Locate every Plasmodium parasite.
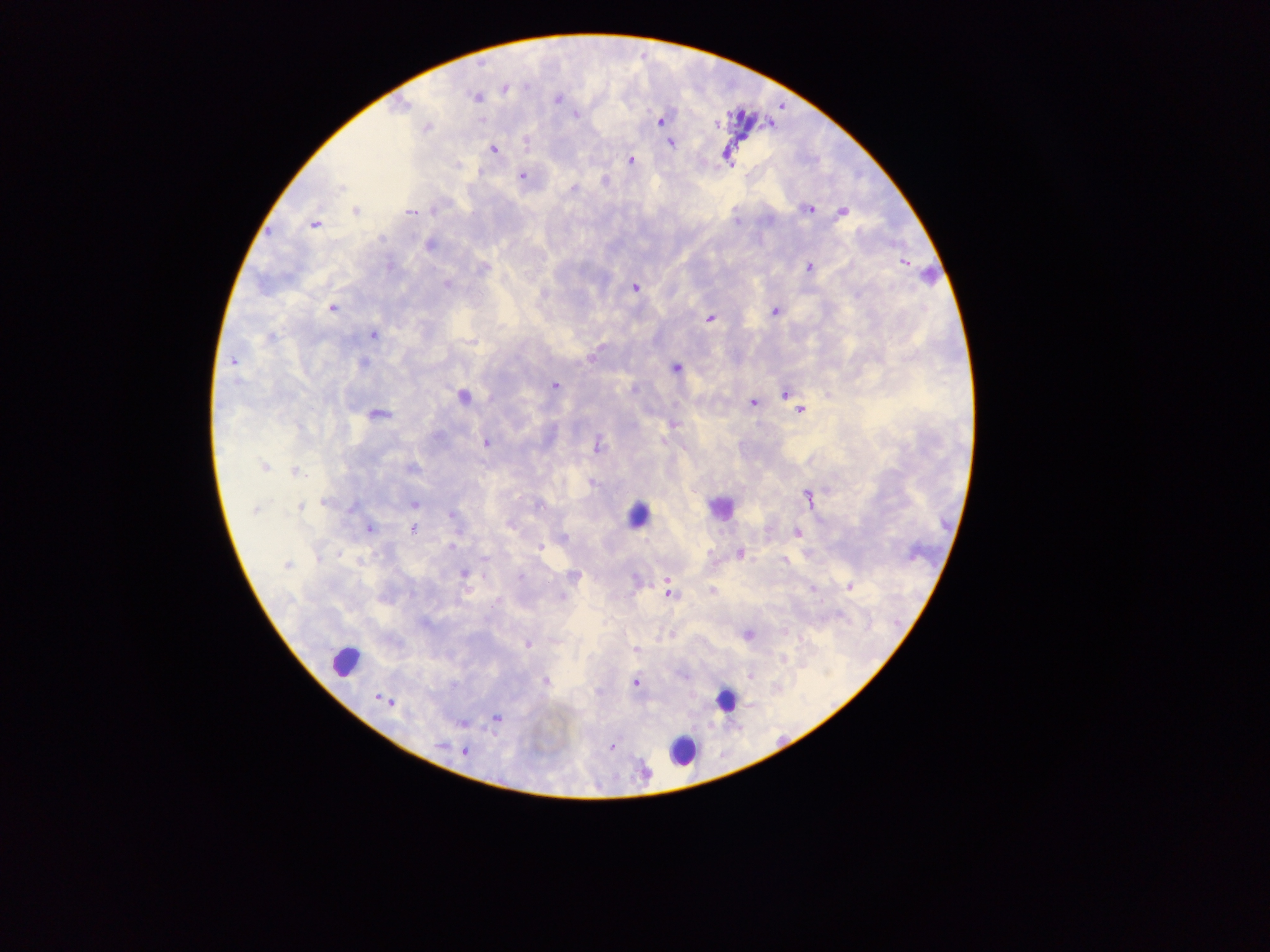

Approximate centers as (x, y) in pixels.
Plasmodium parasites: (505, 88), (476, 97), (558, 98), (401, 106), (576, 115), (481, 120), (661, 120), (717, 124), (427, 128), (526, 144), (671, 144), (494, 150), (727, 155), (631, 160), (480, 171), (522, 176), (341, 188), (573, 188), (809, 209), (355, 211), (410, 212), (843, 212), (735, 221), (315, 224), (429, 245), (904, 262), (809, 266), (389, 267), (483, 268), (447, 286), (635, 288), (332, 309), (774, 311), (710, 318), (374, 335), (270, 338), (471, 341), (591, 356), (232, 361), (363, 363), (675, 368), (236, 381), (555, 385), (785, 394), (462, 397), (752, 403), (799, 410), (377, 414), (673, 424), (436, 436), (662, 442), (486, 443), (597, 447), (264, 466), (411, 468), (295, 472), (592, 483), (808, 497), (324, 502), (414, 505), (537, 505), (300, 507), (353, 507), (255, 510), (452, 514), (509, 526), (370, 529), (413, 529), (796, 532), (562, 538), (451, 546), (540, 547), (339, 554), (740, 554), (783, 560), (287, 565), (463, 573), (485, 576), (574, 576), (520, 577), (667, 581), (849, 587), (466, 588), (711, 590), (668, 594), (562, 596), (498, 601), (748, 634), (527, 644), (635, 649), (783, 659), (749, 676), (545, 681), (635, 683), (378, 697), (386, 700), (391, 702), (497, 717), (462, 724), (440, 745), (612, 747), (465, 751).

Leukocyte locations: (929, 275), (718, 505), (635, 512), (344, 660), (724, 700), (683, 751). Image is 1270×952 pixels. Thick blood smear. Collected in Ghana. Mobile-phone photograph taken through the microscope. One field of view.